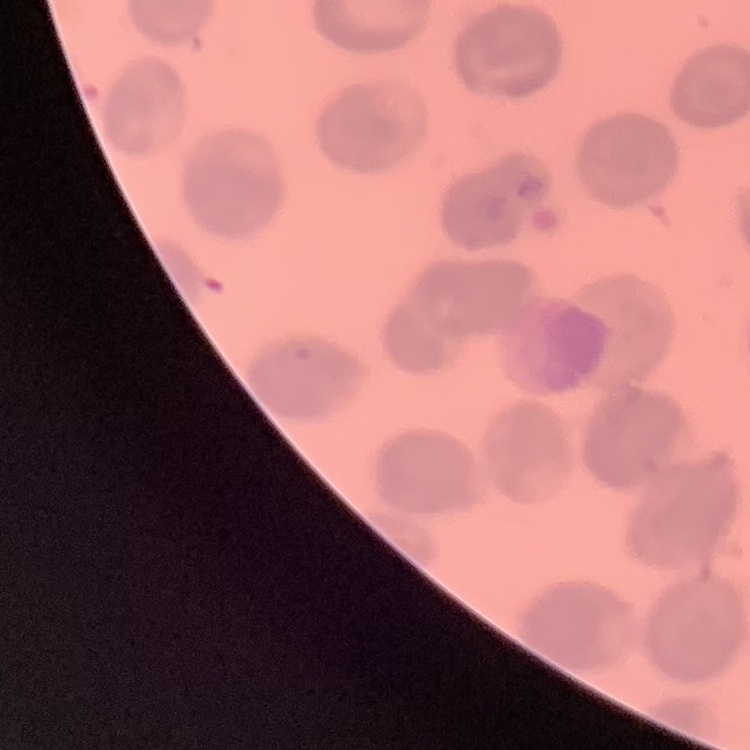

{
  "erythrocyte_morphology": "no rouleaux formation",
  "image_type": "square crop of a larger photomicrograph",
  "preparation": "thin blood smear",
  "stain": "Field's or Giemsa"
}